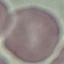
{
  "malaria_status": "uninfected",
  "image_type": "automatically extracted cell patch, resized to 64 × 64 pixels",
  "capture": "smartphone camera at the microscope eyepiece",
  "preparation": "thin blood film",
  "stain": "Giemsa"
}